Assess the morphology of the red blood cells.
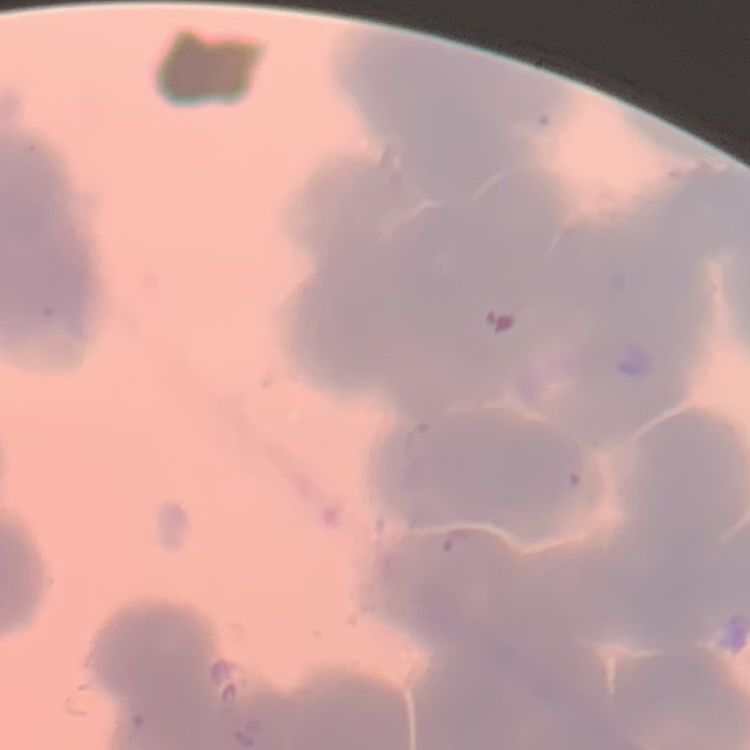
Rouleaux formation.

Summary:
  - Stain: Field's or Giemsa
  - Image type: one tile cut from a larger photomicrograph
  - Preparation: thin peripheral smear